Classify this cell by malaria status.
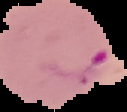

It is parasitized.

image_size: 127×112 pixels
image_type: segmented cell region on a black background
preparation: thin blood smear